Find the red blood cells and label each as Plasmodium falciparum-infected, uninfected, or of indeterminate infection status.
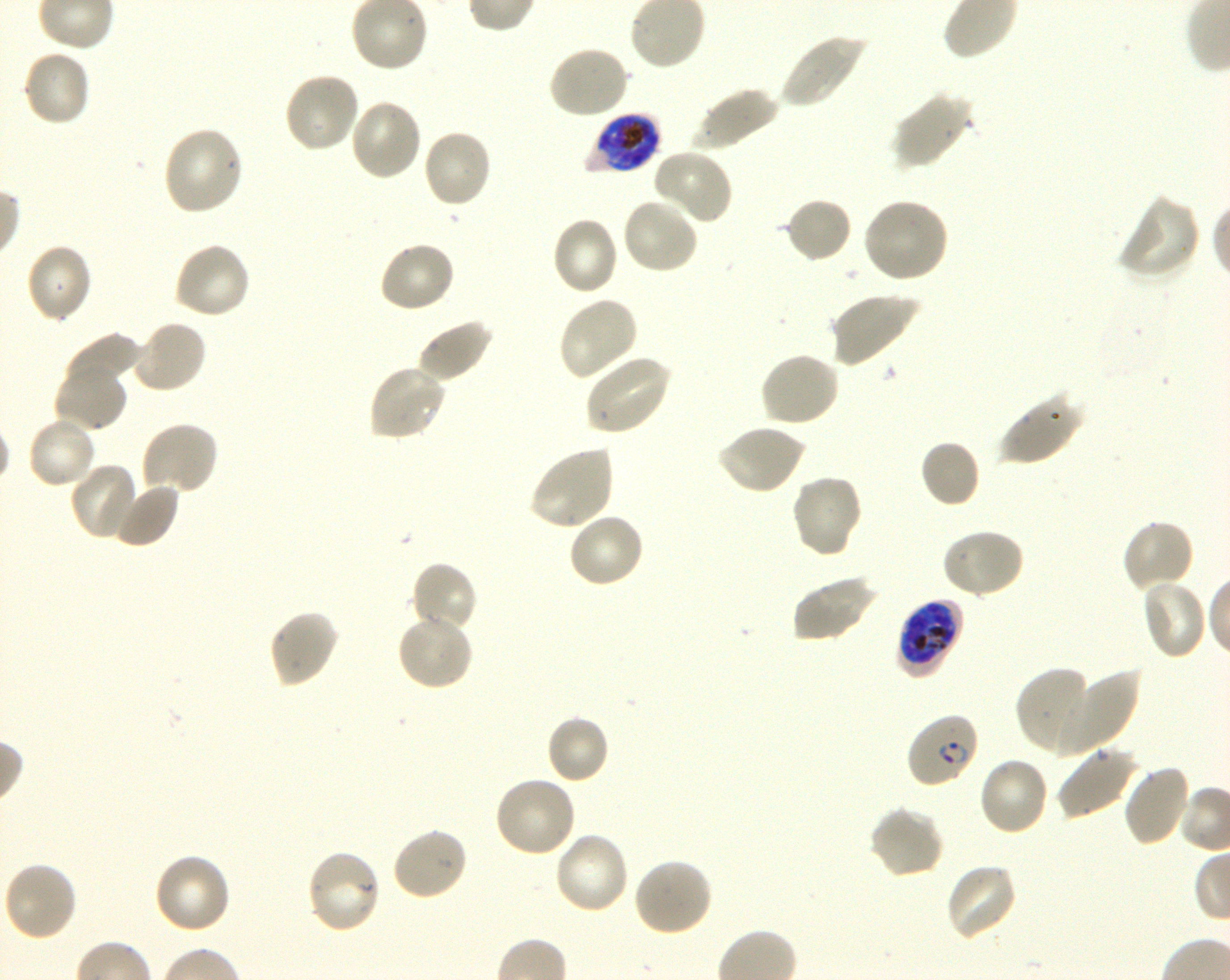

Approximate bounding rectangles given as corner coordinates in pixels from the top-left. Not every red blood cell is marked. A life-cycle stage — or a range of stages, where the recorded stages span more than one — follows each staged infected red blood cell.
Infected red blood cells: (x1=588, y1=113, x2=661, y2=174) late trophozoite to late schizont; (x1=895, y1=597, x2=965, y2=678) late trophozoite to early schizont; (x1=906, y1=712, x2=980, y2=788) ring.
Uninfected red blood cells: (x1=777, y1=33, x2=867, y2=109), (x1=547, y1=45, x2=631, y2=120), (x1=22, y1=48, x2=91, y2=128), (x1=283, y1=72, x2=361, y2=154), (x1=691, y1=86, x2=779, y2=152), (x1=891, y1=92, x2=973, y2=170), (x1=349, y1=99, x2=425, y2=182), (x1=161, y1=126, x2=246, y2=216), (x1=421, y1=128, x2=493, y2=209), (x1=652, y1=149, x2=733, y2=225), (x1=1116, y1=194, x2=1201, y2=283), (x1=784, y1=196, x2=853, y2=263), (x1=862, y1=197, x2=949, y2=284), (x1=621, y1=198, x2=700, y2=276), (x1=550, y1=215, x2=619, y2=297), (x1=378, y1=240, x2=456, y2=314), (x1=172, y1=241, x2=252, y2=320), (x1=25, y1=243, x2=93, y2=324), (x1=829, y1=292, x2=918, y2=368), (x1=557, y1=296, x2=639, y2=382), (x1=416, y1=318, x2=494, y2=384), (x1=131, y1=319, x2=208, y2=395), (x1=62, y1=331, x2=140, y2=394), (x1=758, y1=351, x2=840, y2=427), (x1=582, y1=355, x2=672, y2=436), (x1=53, y1=362, x2=129, y2=433), (x1=366, y1=363, x2=448, y2=442), (x1=996, y1=394, x2=1083, y2=467), (x1=26, y1=415, x2=97, y2=491), (x1=139, y1=420, x2=220, y2=496), (x1=716, y1=423, x2=806, y2=495), (x1=919, y1=439, x2=981, y2=509), (x1=529, y1=444, x2=615, y2=532), (x1=68, y1=462, x2=140, y2=541), (x1=790, y1=474, x2=863, y2=558), (x1=112, y1=480, x2=181, y2=549), (x1=566, y1=511, x2=645, y2=589), (x1=1121, y1=518, x2=1196, y2=592), (x1=940, y1=527, x2=1025, y2=600), (x1=409, y1=561, x2=479, y2=634), (x1=791, y1=574, x2=878, y2=643), (x1=1139, y1=579, x2=1209, y2=660), (x1=267, y1=609, x2=340, y2=690), (x1=396, y1=612, x2=475, y2=691), (x1=1016, y1=667, x2=1097, y2=755), (x1=1048, y1=669, x2=1139, y2=754), (x1=545, y1=714, x2=610, y2=785), (x1=1056, y1=745, x2=1140, y2=819), (x1=978, y1=756, x2=1050, y2=836), (x1=1121, y1=763, x2=1193, y2=848), (x1=492, y1=776, x2=577, y2=859), (x1=868, y1=804, x2=944, y2=880), (x1=390, y1=826, x2=469, y2=902), (x1=552, y1=831, x2=631, y2=915), (x1=306, y1=848, x2=383, y2=935), (x1=152, y1=852, x2=232, y2=936), (x1=632, y1=856, x2=713, y2=938), (x1=2, y1=861, x2=78, y2=943), (x1=944, y1=862, x2=1018, y2=942).
No red blood cells of indeterminate infection status observed.

field of view = single
stain = Giemsa
culture = in-vitro Plasmodium falciparum strain 3D7, shaking
preparation = thin blood film
objective = 100x, oil immersion, numerical aperture 1.30
image size = 1230×980 pixels
donor blood group = O+